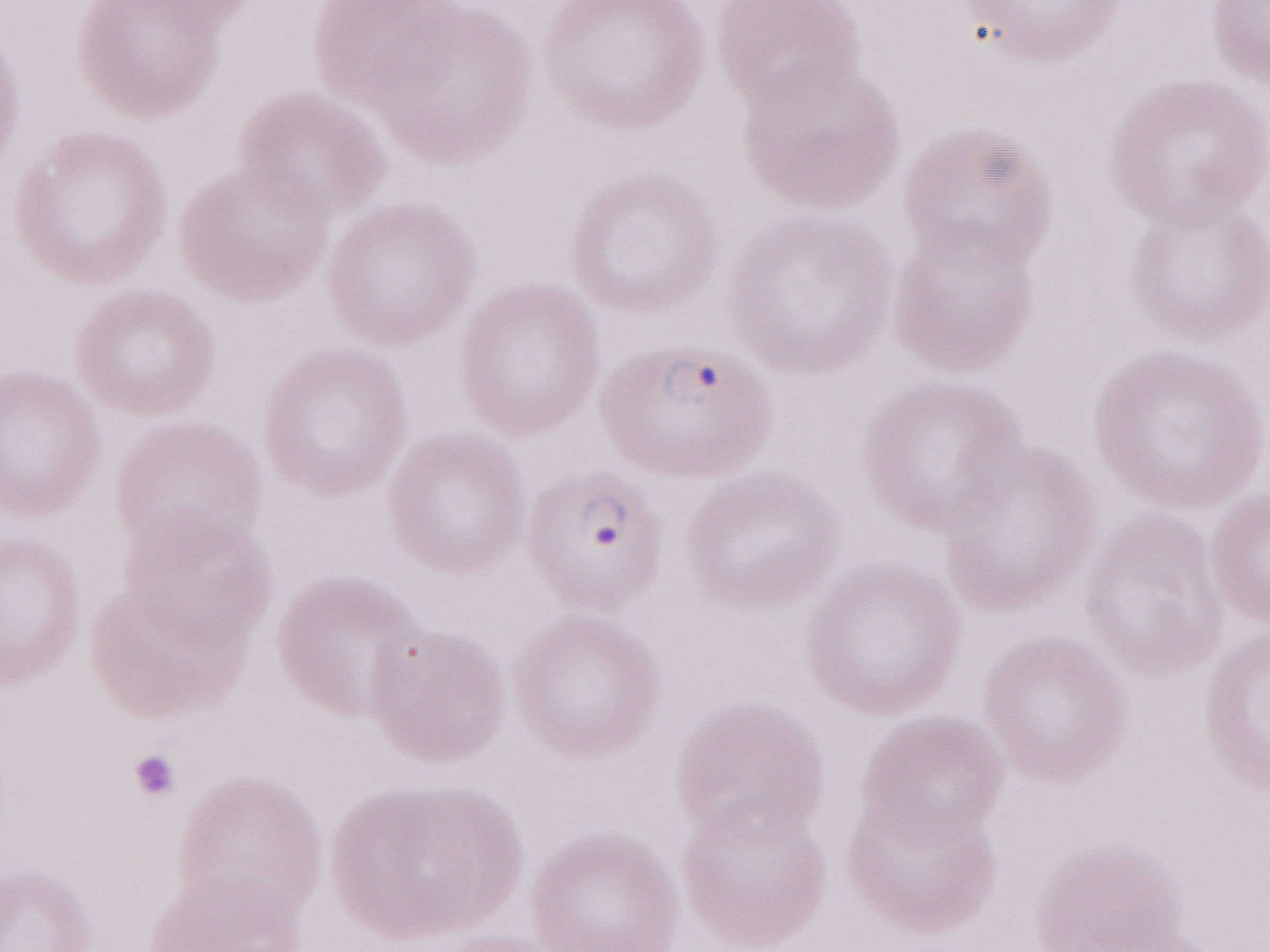 Image is 1270×952 pixels. Single field of view. Patient-level malaria diagnosis: positive. Olympus BX43 microscope, Olympus DP73 camera. 1,000x magnification. Thin blood smear. May-Grünwald-Giemsa (MGG) stain.